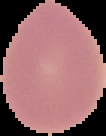

image type = cell region segmented out of the field of view; surrounding area masked to black
preparation = thin blood smear
image size = 106×136 pixels
result = no malaria parasites detected